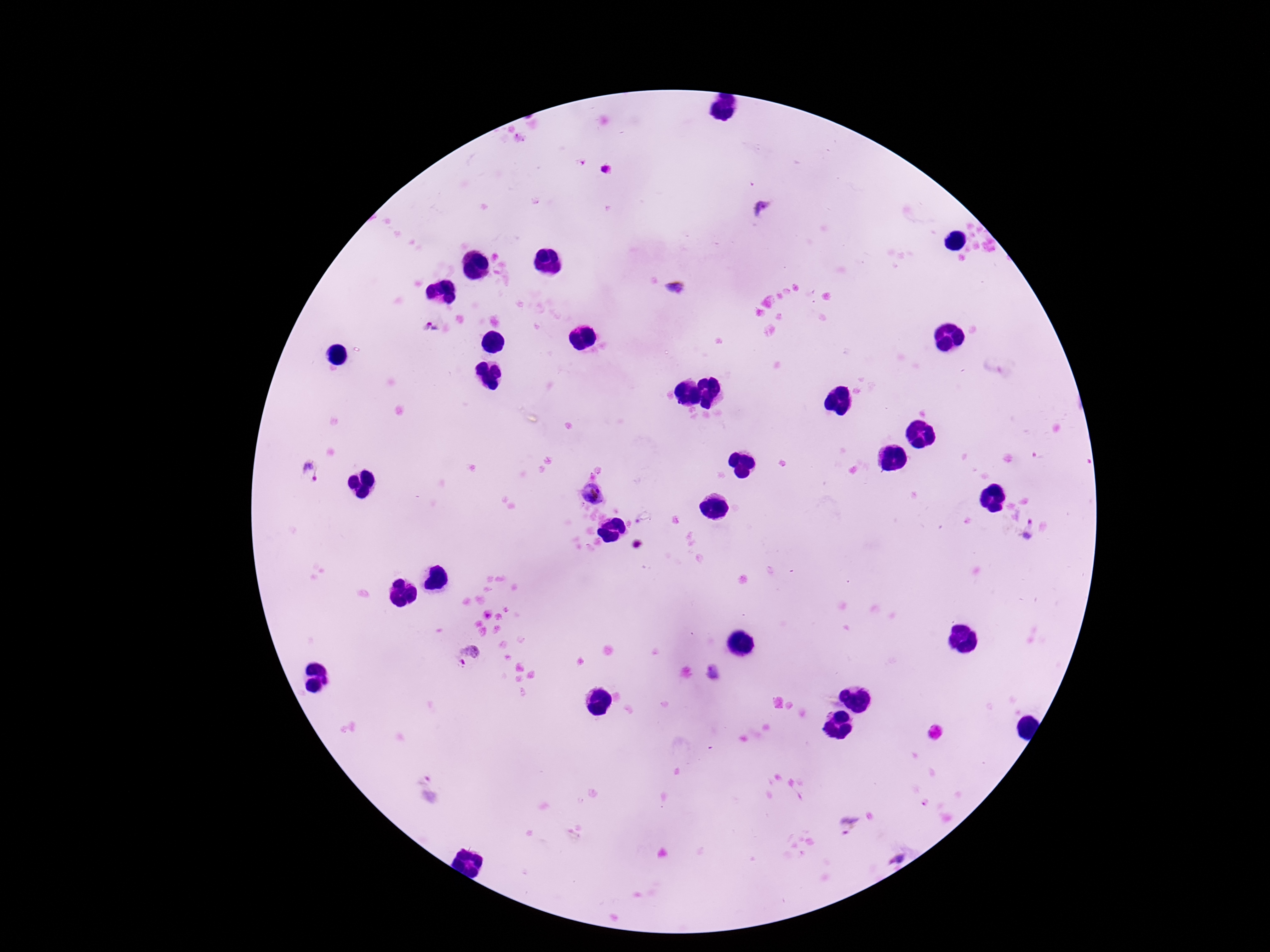

patient_malaria_status: infected
magnification: 100x
image_size: 1270×952 pixels
preparation: thick blood film
stain: Giemsa
capture: smartphone camera through the microscope eyepiece
plasmodium_parasite_locations: 'approximate centers as {x, y} in pixels: {607, 171}, {761, 208}, {676, 290}, {431, 328}, {311, 472}, {593, 493}, {1027, 530}, {469, 657}, {712, 673}, {848, 825}, {895, 855}'
field_of_view: single